Locate and identify every blood parasite.
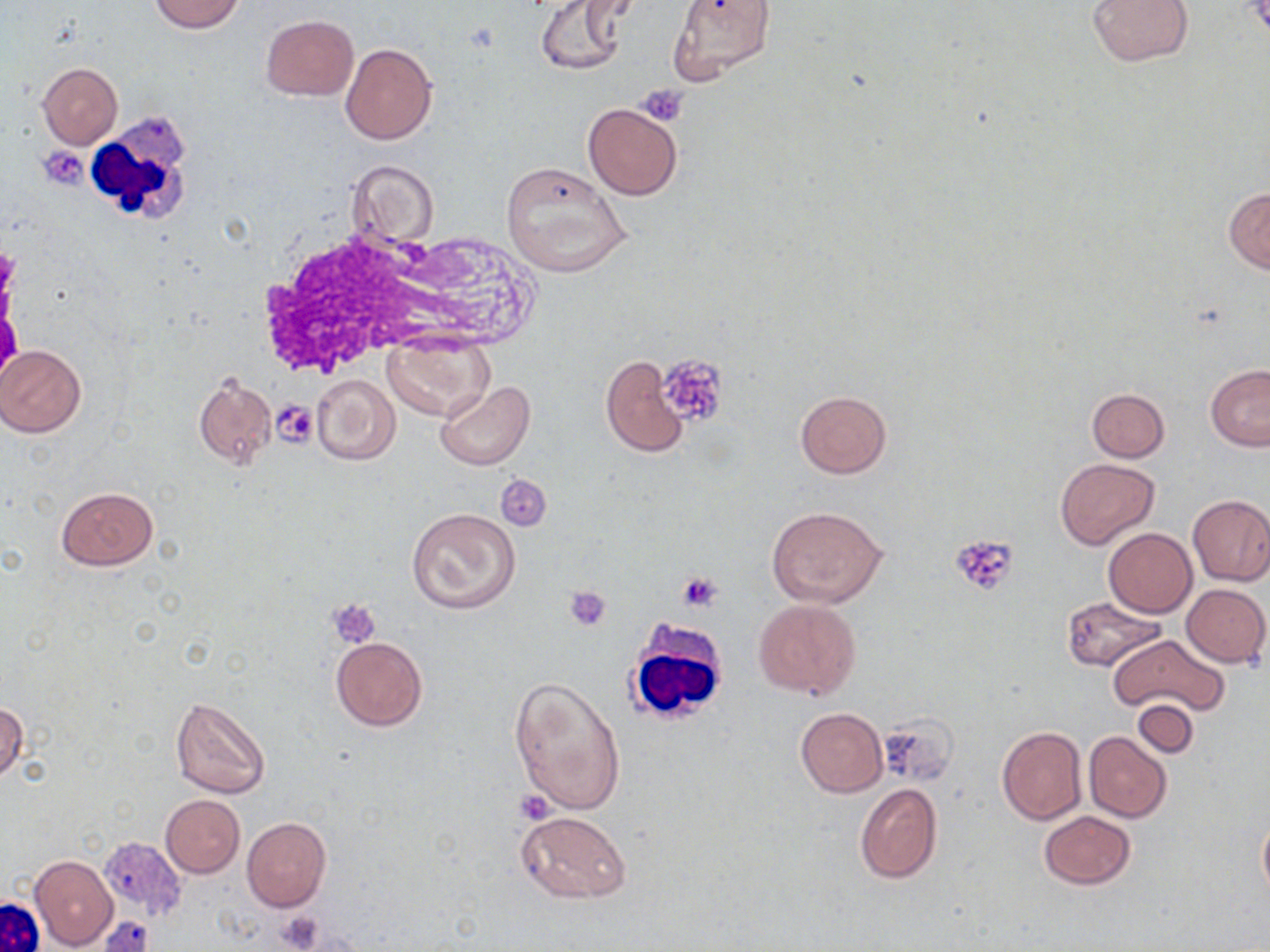

No blood parasites seen.

Summary:
  - Coordinate format: approximate bounding boxes as [x1, y1, x2, y2] in pixels
  - Platelet locations: [637, 82, 690, 125], [38, 144, 90, 189], [0, 305, 22, 380], [653, 352, 726, 424], [271, 398, 320, 447], [495, 475, 553, 533], [950, 534, 1019, 595], [677, 571, 724, 612], [564, 585, 612, 632], [326, 598, 382, 649], [514, 789, 555, 824], [274, 910, 325, 952], [100, 917, 152, 952]
  - White blood cell locations: [84, 118, 199, 234], [253, 225, 476, 377], [623, 619, 731, 726]
  - Uninfected red blood cell locations: [148, 0, 244, 33], [538, 0, 632, 76], [666, 0, 774, 84], [1086, 0, 1194, 67], [261, 15, 358, 101], [340, 43, 437, 143], [38, 63, 123, 149], [582, 104, 683, 199], [346, 159, 438, 249], [500, 161, 632, 278], [1224, 187, 1270, 273], [383, 335, 493, 421], [0, 344, 86, 437], [600, 354, 690, 459], [1205, 365, 1270, 451], [193, 370, 277, 470], [311, 373, 400, 465], [435, 381, 536, 469], [1087, 388, 1170, 462], [794, 391, 892, 479], [1053, 458, 1159, 550], [56, 486, 159, 571], [1187, 495, 1270, 587], [765, 505, 888, 608], [407, 508, 520, 615], [1103, 527, 1197, 619], [1080, 539, 1187, 667], [1181, 583, 1270, 668], [1061, 597, 1166, 671], [753, 598, 861, 700], [1108, 634, 1230, 717], [331, 637, 426, 731], [509, 673, 627, 816], [170, 697, 270, 799], [1131, 698, 1199, 758], [0, 701, 26, 782], [794, 708, 887, 796], [873, 714, 956, 786], [996, 724, 1086, 825], [1083, 731, 1171, 822], [854, 783, 942, 884], [160, 795, 244, 878], [518, 810, 632, 905], [1038, 811, 1136, 889], [1257, 812, 1270, 903], [242, 816, 332, 913], [29, 855, 117, 951]
  - Slide-level diagnosis: no evidence of blood parasites
  - Magnification: 1000x
  - Preparation: thin blood smear
  - Modality: optical microscopy
  - Stain: May-Grünwald-Giemsa
  - Image size: 1270×952 pixels
  - Field of view: one of a larger specimen